Classify this cell by malaria status.
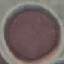

Uninfected.

Summary:
  - Image type: automatically extracted cell patch, resized to 64 × 64 pixels
  - Stain: Giemsa
  - Preparation: thin smear
  - Capture: smartphone camera at the microscope eyepiece